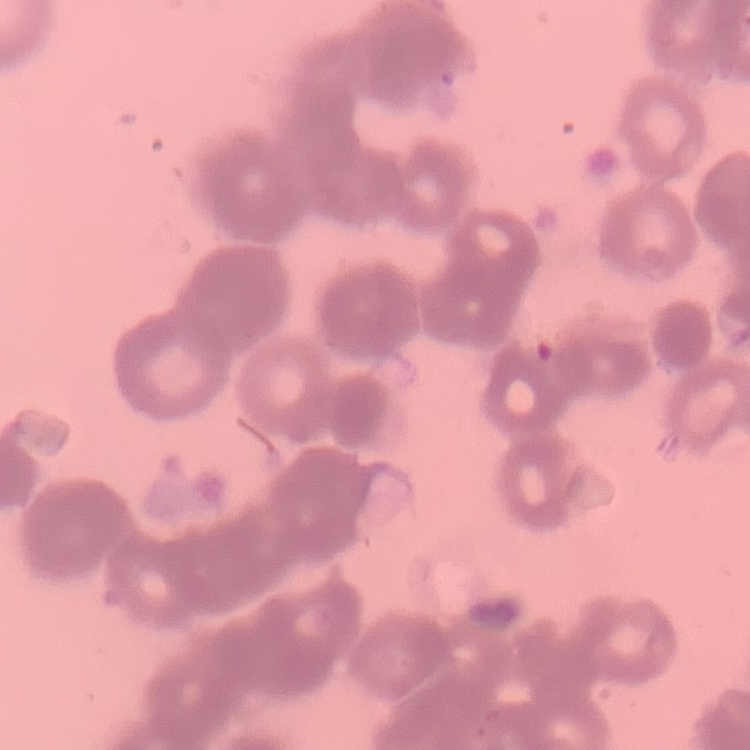
{
  "erythrocyte_morphology": "rouleaux formation",
  "preparation": "thin blood smear",
  "stain": "Field's or Giemsa",
  "image_type": "square crop of a larger photomicrograph"
}